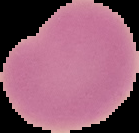
malaria status = uninfected
image size = 139×133 pixels
preparation = thin blood film
image type = segmented cell region with the area outside set to black